Rate the background quality.
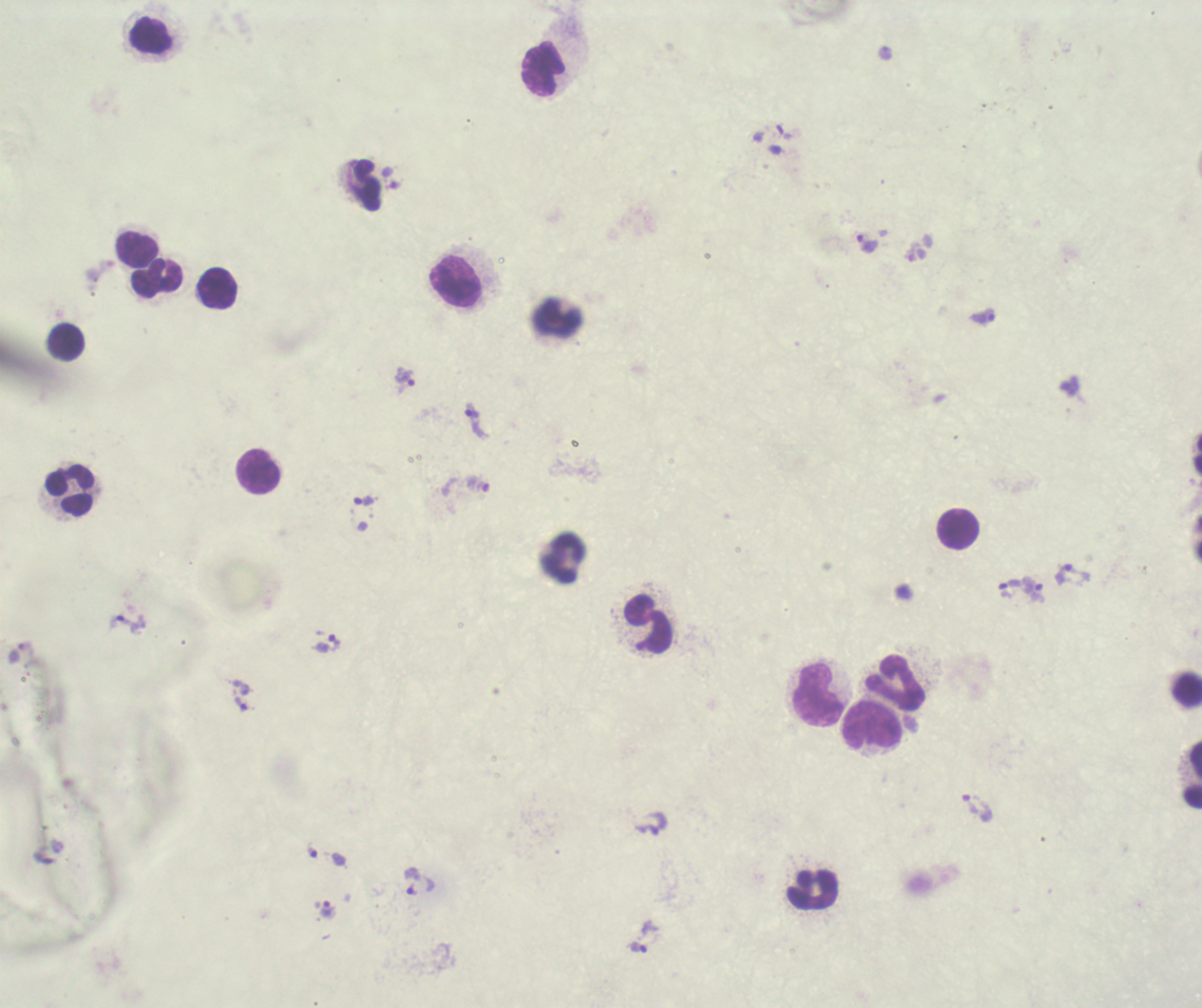

It is poor.

Approximate object centers, in pixels from the top-left corner.
Summary:
  - Leukocyte locations: (x=149, y=36), (x=543, y=69), (x=366, y=185), (x=136, y=248), (x=155, y=280), (x=455, y=281), (x=214, y=288), (x=65, y=343), (x=258, y=473), (x=69, y=490), (x=957, y=529), (x=564, y=556), (x=648, y=625), (x=895, y=683), (x=1187, y=689), (x=818, y=695), (x=871, y=726), (x=1192, y=775), (x=811, y=889)
  - Trophozoite locations: (x=866, y=242), (x=981, y=317), (x=406, y=375), (x=475, y=421), (x=364, y=500), (x=1072, y=574), (x=1010, y=589), (x=1034, y=590), (x=125, y=623), (x=326, y=643), (x=241, y=703), (x=968, y=804), (x=312, y=852), (x=411, y=890), (x=328, y=910), (x=637, y=947)
  - Image size: 1202×1008 pixels
  - Coloration quality: bad
  - Context: previously used in an actual diagnosis
  - Field of view: one from this slide
  - Stain: Romanowsky
  - Preparation: thick blood smear
  - Magnification: 100x
  - Result: Plasmodium parasites detected